Report the malaria status of this cell.
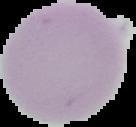

Uninfected.

From a thin blood film. The area outside the segmented cell region is set to black. Image is 136×127 pixels.